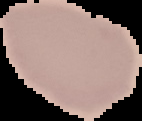
{
  "preparation": "thin blood smear",
  "image_type": "segmented cell region with the area outside set to black",
  "malaria_status": "uninfected",
  "image_size": "142×121 pixels"
}